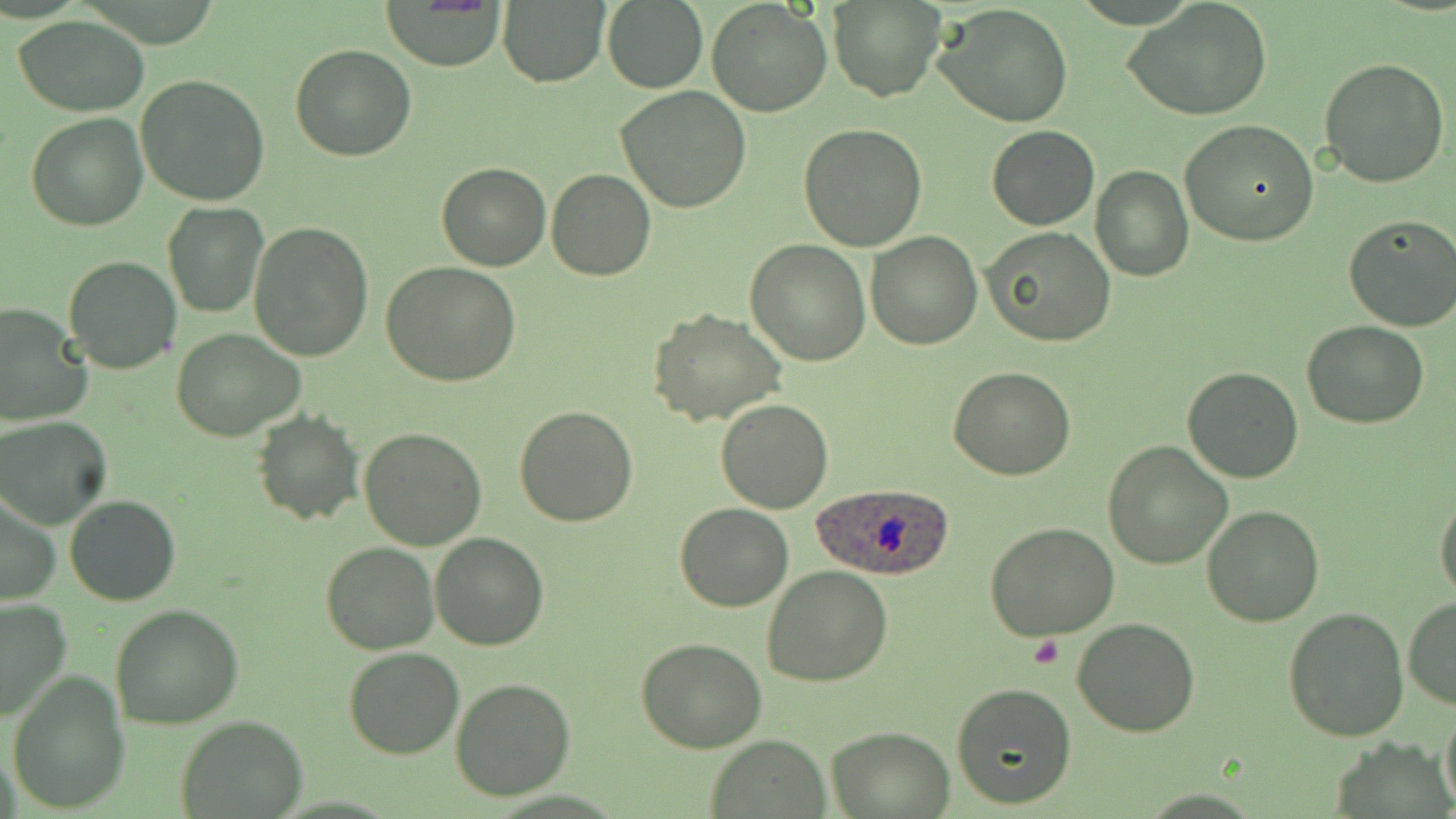
Approximate bounding boxes as (x1, y1, x2, y2) in pixels. Uninfected red blood cell locations: (498, 0, 611, 88), (706, 0, 833, 118), (1124, 0, 1273, 123), (830, 1, 944, 101), (384, 2, 508, 71), (602, 2, 708, 91), (934, 4, 1074, 127), (13, 18, 152, 116), (290, 45, 417, 162), (1318, 56, 1451, 189), (136, 74, 272, 207), (616, 86, 751, 213), (26, 111, 148, 230), (1180, 119, 1318, 245), (797, 122, 927, 251), (986, 126, 1099, 230), (436, 163, 552, 272), (1091, 166, 1192, 281), (545, 168, 656, 282), (162, 201, 269, 317), (1340, 213, 1456, 333), (250, 220, 376, 361), (983, 227, 1117, 349), (866, 230, 982, 349), (745, 240, 871, 367), (62, 254, 182, 374), (381, 261, 520, 387), (0, 301, 93, 427), (646, 307, 787, 427), (1301, 320, 1429, 430), (172, 328, 304, 442), (949, 365, 1077, 480), (1183, 365, 1303, 483), (715, 398, 833, 513), (513, 406, 639, 527), (251, 411, 363, 526), (1, 416, 115, 532), (359, 426, 489, 551), (1103, 440, 1232, 570), (1, 492, 61, 606), (65, 494, 180, 606), (1435, 496, 1456, 602), (677, 504, 793, 612), (1202, 505, 1325, 626), (983, 524, 1120, 642), (430, 532, 549, 651), (320, 541, 438, 655), (762, 564, 893, 687), (1403, 596, 1456, 709), (0, 597, 73, 723), (110, 604, 243, 730), (1281, 606, 1409, 741), (1071, 616, 1201, 737), (635, 636, 769, 753), (343, 646, 465, 760), (6, 674, 129, 811), (450, 678, 575, 802), (951, 683, 1076, 811), (1440, 699, 1456, 814), (176, 714, 308, 817), (825, 725, 954, 817), (707, 736, 832, 817). Plasmodium ovale-infected red blood cell locations: (810, 482, 957, 583). Platelet locations: (1023, 637, 1064, 667). Slide-level diagnosis: Plasmodium ovale. Image is 1456×819 pixels. Light microscopy. One field of a larger specimen. Captured at 1000x magnification. Thin blood film. May-Grünwald-Giemsa stain.